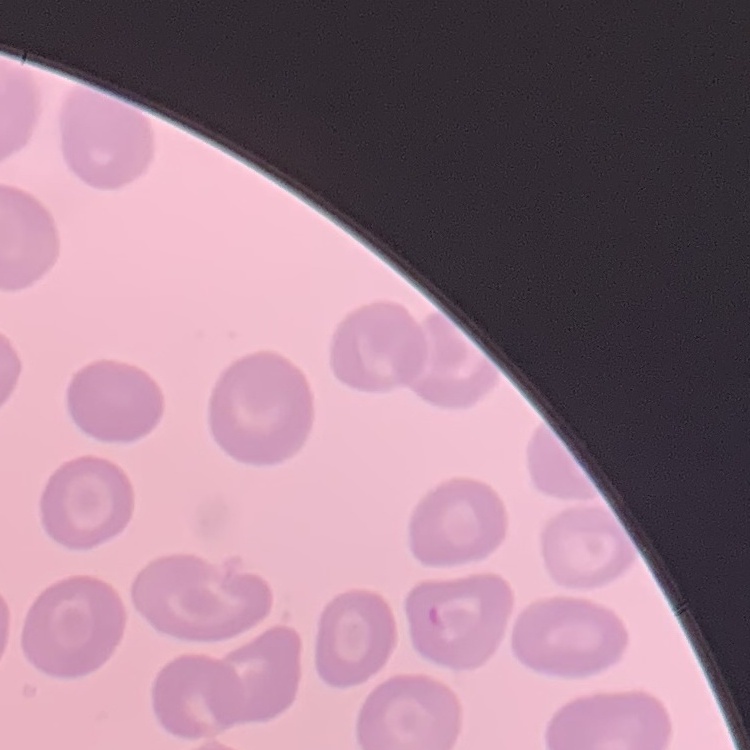

Summary:
  - Erythrocyte morphology: no rouleaux formation
  - Image type: square crop of a larger photomicrograph
  - Preparation: thin blood smear
  - Stain: Field's or Giemsa